Locate every blood parasite and identify its species.
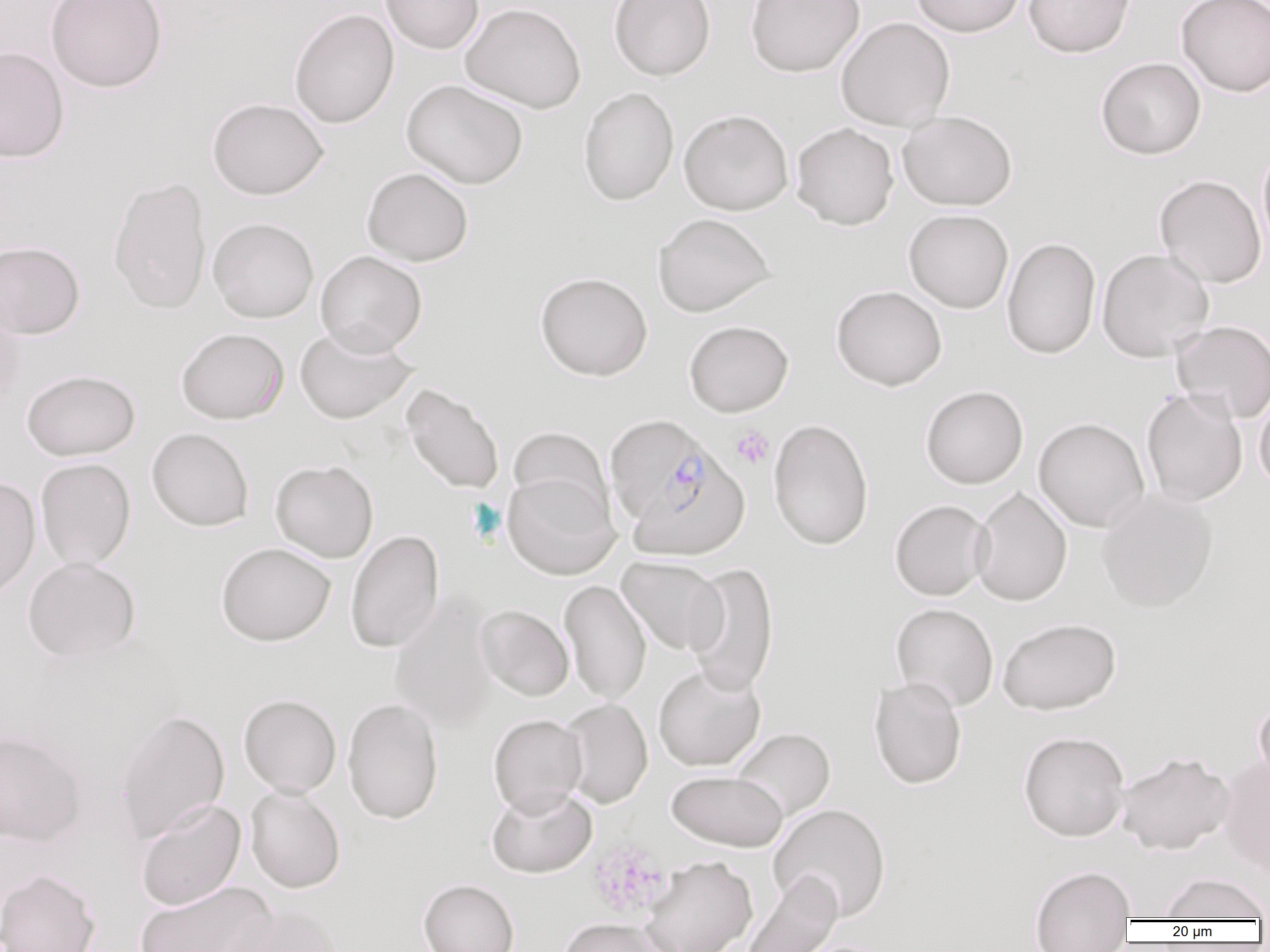

Approximate bounding boxes as [x1, y1, x2, y2] in pixels.
Plasmodium falciparum-infected red blood cells: [604, 415, 714, 526], [627, 450, 750, 562].
No Plasmodium ovale, Plasmodium malariae, Plasmodium vivax, Babesia divergens, or Trypanosoma brucei observed.

{
  "slide_level_diagnosis": "Plasmodium falciparum",
  "magnification": "1000x",
  "modality": "optical microscopy",
  "preparation": "thin blood film",
  "image_size": "1270×952 pixels",
  "field_of_view": "single",
  "uninfected_red_blood_cell_locations": "approximate bounding boxes as [x1, y1, x2, y2] in pixels: [45, 0, 167, 93], [379, 0, 485, 54], [609, 0, 716, 81], [745, 0, 865, 77], [909, 0, 1025, 37], [1023, 0, 1136, 58], [1175, 0, 1270, 98], [460, 2, 586, 114], [288, 8, 399, 129], [835, 16, 955, 131], [0, 46, 69, 163], [1095, 57, 1206, 160], [401, 79, 528, 189], [578, 87, 679, 206], [207, 97, 329, 200], [679, 109, 794, 215], [898, 111, 1017, 210], [790, 122, 900, 230], [1257, 145, 1270, 263], [361, 166, 474, 266], [1154, 174, 1267, 289], [108, 176, 212, 315], [903, 208, 1014, 313], [652, 212, 776, 317], [208, 217, 319, 322], [1001, 237, 1101, 359], [0, 240, 85, 339], [1096, 247, 1215, 362], [315, 250, 427, 355], [534, 271, 653, 381], [830, 285, 947, 391], [0, 296, 26, 417], [683, 320, 794, 417], [1171, 321, 1270, 423], [294, 323, 417, 424], [176, 327, 289, 425], [21, 369, 141, 460], [401, 383, 505, 494], [920, 385, 1029, 489], [1254, 387, 1270, 495], [1141, 388, 1248, 507], [1033, 417, 1150, 532], [768, 418, 874, 550], [507, 426, 615, 524], [146, 427, 254, 531], [35, 457, 136, 570], [269, 459, 379, 562], [502, 470, 620, 579], [0, 475, 41, 602], [971, 486, 1073, 606], [1096, 487, 1218, 612], [889, 499, 993, 600], [345, 530, 444, 653], [215, 542, 336, 646], [22, 556, 141, 663], [617, 556, 727, 655], [684, 562, 780, 697], [559, 579, 651, 704], [389, 593, 498, 733], [890, 603, 999, 712], [476, 604, 574, 701], [997, 617, 1122, 715], [653, 664, 766, 771], [868, 676, 967, 790], [238, 694, 342, 797], [1253, 695, 1270, 790], [342, 697, 443, 824], [560, 698, 653, 808], [115, 709, 230, 842], [488, 714, 587, 816], [732, 727, 836, 821], [0, 729, 87, 847], [1018, 730, 1130, 842], [1116, 751, 1236, 855], [1218, 756, 1270, 876], [666, 770, 788, 851], [486, 784, 597, 878], [245, 785, 346, 893], [135, 798, 245, 910], [768, 803, 891, 922], [641, 856, 757, 952], [1029, 864, 1136, 951], [0, 869, 101, 952], [740, 870, 843, 952], [1158, 873, 1269, 921], [418, 878, 519, 952], [135, 880, 276, 952], [222, 904, 345, 952], [558, 917, 670, 952]",
  "platelet_locations": "approximate bounding boxes as [x1, y1, x2, y2] in pixels: [731, 425, 774, 469], [588, 840, 670, 919]"
}